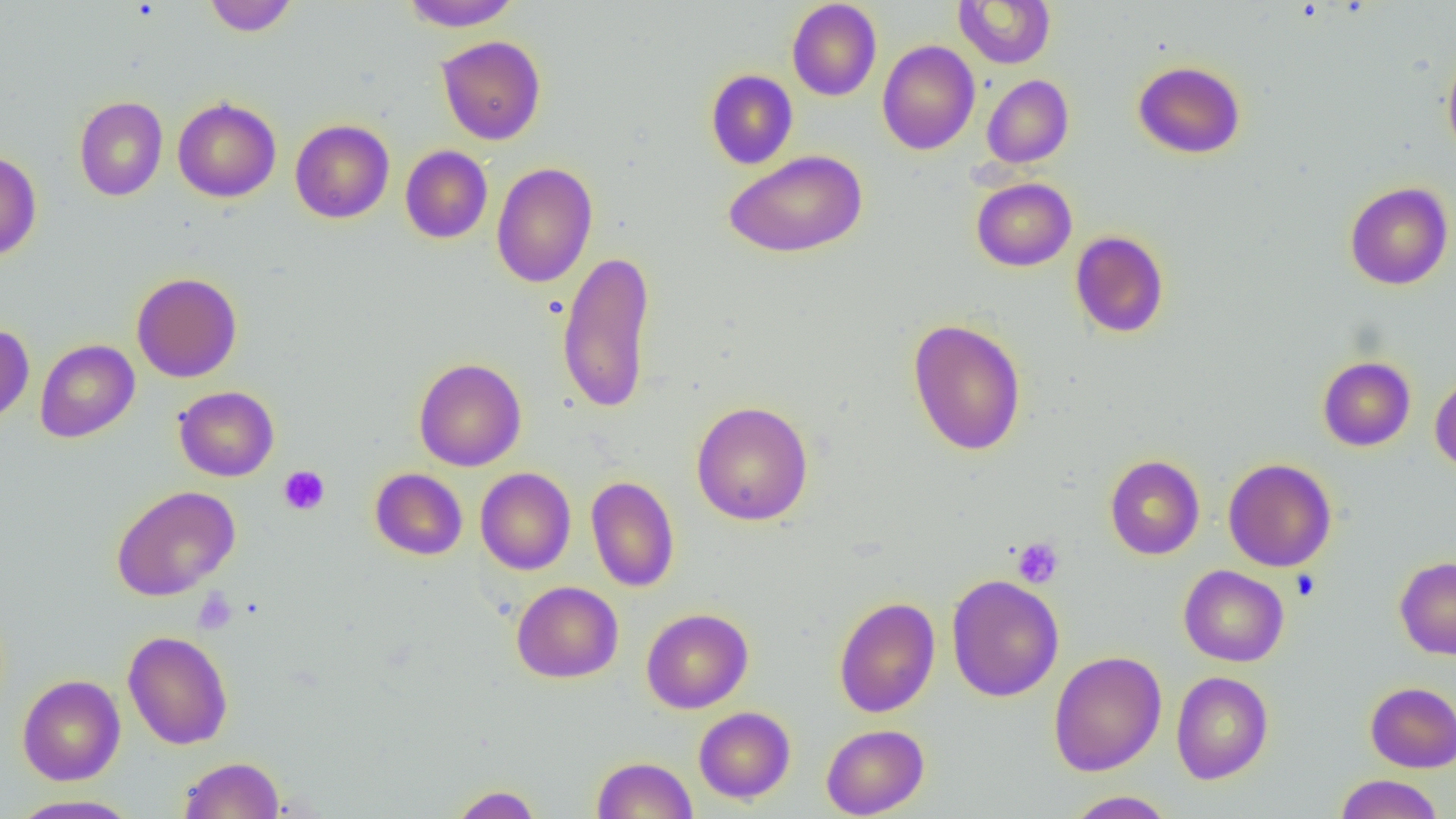

Approximate bounding boxes as (x1,y1)-(x2,y2) corner pairs in pixels. Platelet locations: (279,465)-(330,515), (1011,538)-(1063,588), (1290,569)-(1321,600), (192,589)-(237,634). Uninfected red blood cell locations: (204,0)-(299,37), (399,0)-(521,31), (786,0)-(882,101), (953,0)-(1055,68), (436,35)-(546,145), (877,40)-(980,155), (1442,52)-(1456,159), (1133,60)-(1246,159), (705,69)-(798,169), (982,74)-(1074,168), (74,96)-(168,201), (173,97)-(281,202), (290,119)-(394,223), (400,145)-(492,244), (724,150)-(868,258), (0,151)-(41,261), (491,162)-(597,288), (971,177)-(1077,272), (1344,181)-(1454,290), (1070,230)-(1170,338), (557,249)-(657,414), (131,272)-(242,382), (907,318)-(1027,456), (0,324)-(35,426), (35,339)-(139,443), (1317,356)-(1416,451), (414,358)-(526,471), (1430,375)-(1456,474), (174,385)-(279,481), (691,400)-(814,526), (1104,454)-(1205,560), (1223,458)-(1336,572), (475,467)-(576,575), (370,468)-(467,560), (585,476)-(680,592), (112,485)-(241,601), (1394,557)-(1456,659), (1178,565)-(1289,667), (946,574)-(1064,702), (512,581)-(623,683), (833,596)-(940,717), (641,608)-(753,713), (122,630)-(233,750), (1049,651)-(1166,776), (1171,671)-(1273,784), (17,674)-(125,785), (1365,681)-(1456,773), (694,707)-(796,803), (820,724)-(929,818), (179,756)-(285,818), (592,756)-(697,818), (1335,774)-(1444,818), (448,784)-(543,818), (1064,790)-(1177,818), (8,794)-(143,818). Slide-level diagnosis: negative for blood parasites. Thin blood film. Light microscopy. 1000x magnification. Single field of view. Image is 1456×819 pixels.